State which parasite is depicted.
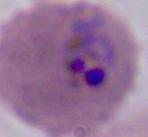
This is Plasmodium.

modality: photomicrograph
magnification: 400x or 1000x